Draw a bounding box around every leukocyte (white blood cell).
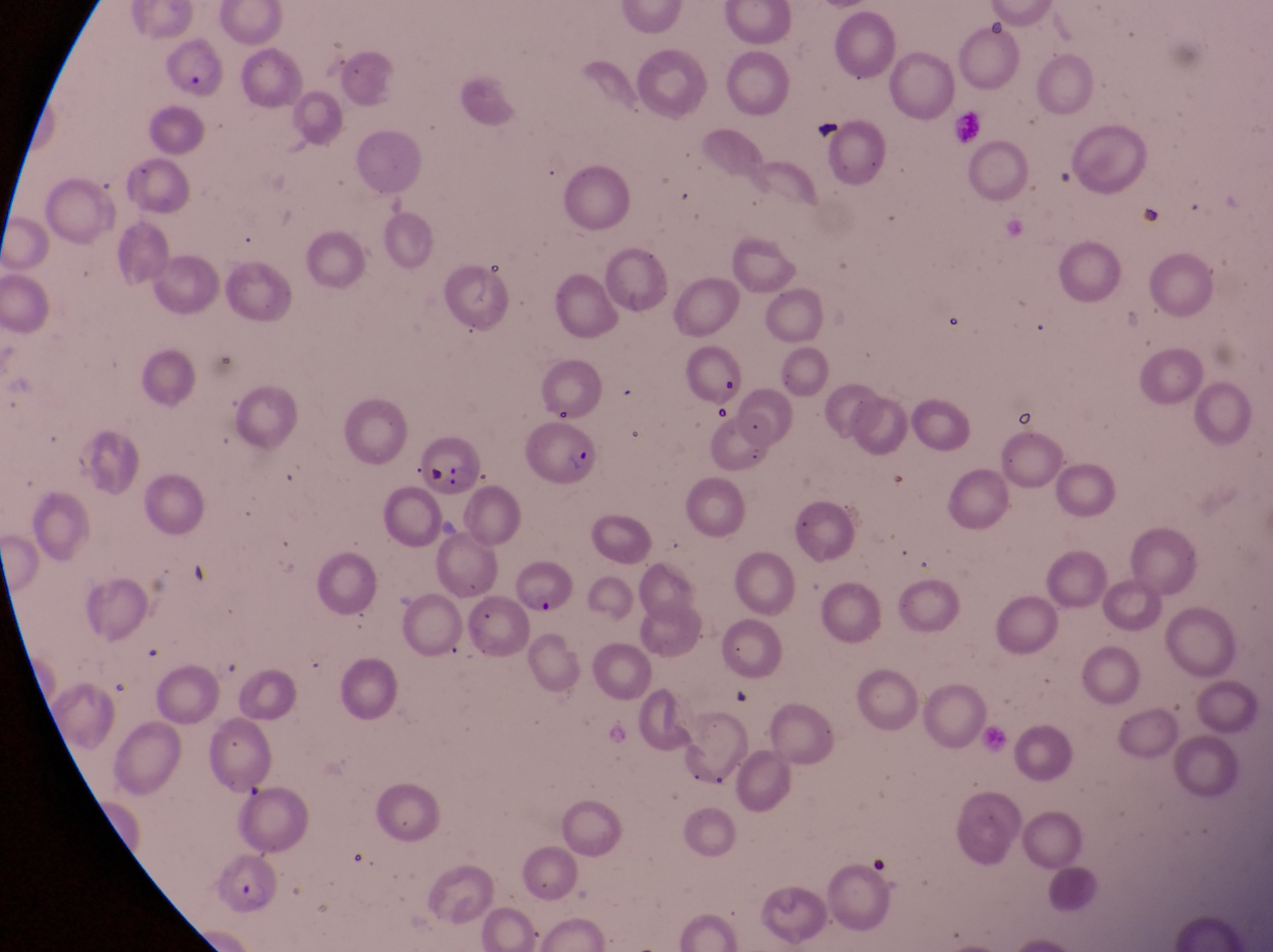
Approximate bounding boxes as left top right bottom in pixels.
Leukocytes: 945 107 987 145.

country: Uganda
parasitised_red_blood_cell_locations: 'approximate bounding boxes as left top right bottom in pixels: 524 419 604 491; 415 435 487 498; 509 549 589 619; 215 852 277 919'
image_size: 1273×952 pixels
artifact_platelet_like_body_stain_precipitate_or_debris_locations: 'approximate bounding boxes as left top right bottom in pixels: 704 402 737 425; 1011 402 1036 435'
capture: smartphone photograph through the eyepiece of an Olympus CX-23 microscope
field_of_view: single
preparation: thin blood smear
magnification: 1000x